Assess the morphology of the red blood cells.
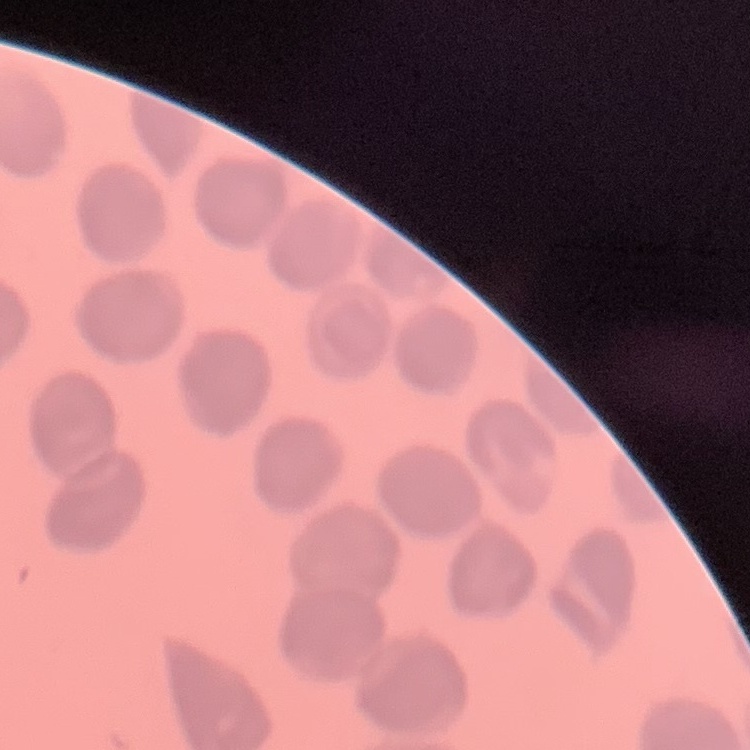

No rouleaux formation.

Summary:
  - Stain: Field's or Giemsa
  - Preparation: thin peripheral smear
  - Image type: one tile cut from a larger photomicrograph